Assess this cell for malaria.
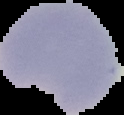

It is parasitized.

{
  "image_size": "124×115 pixels",
  "image_type": "segmented cell region with the area outside set to black",
  "preparation": "thin blood film"
}